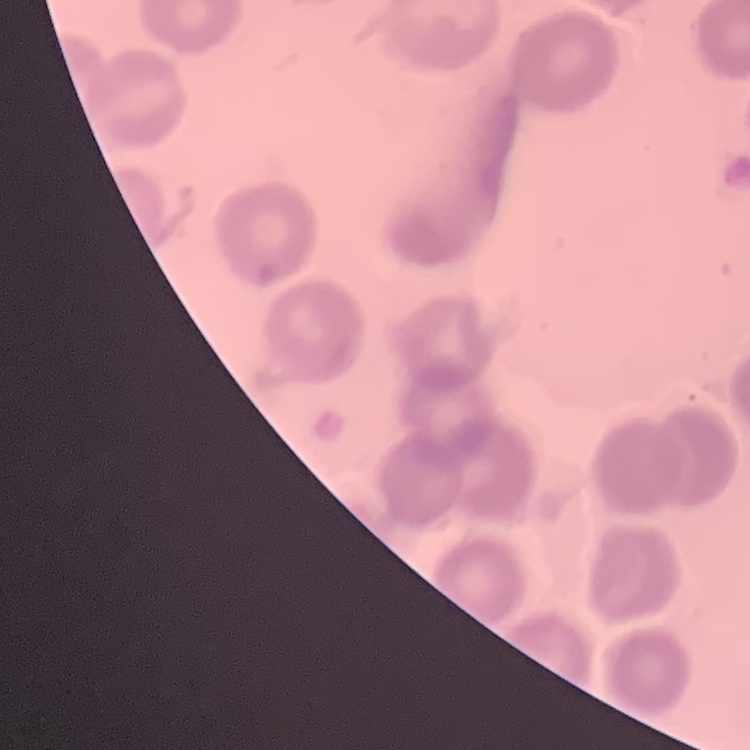 The red blood cells exhibit no rouleaux formation. Square crop of a larger photomicrograph. Stained with either Field's or Giemsa. Thin blood smear.